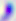

modality = micrograph
magnification = 400x
identification = Toxoplasma gondii